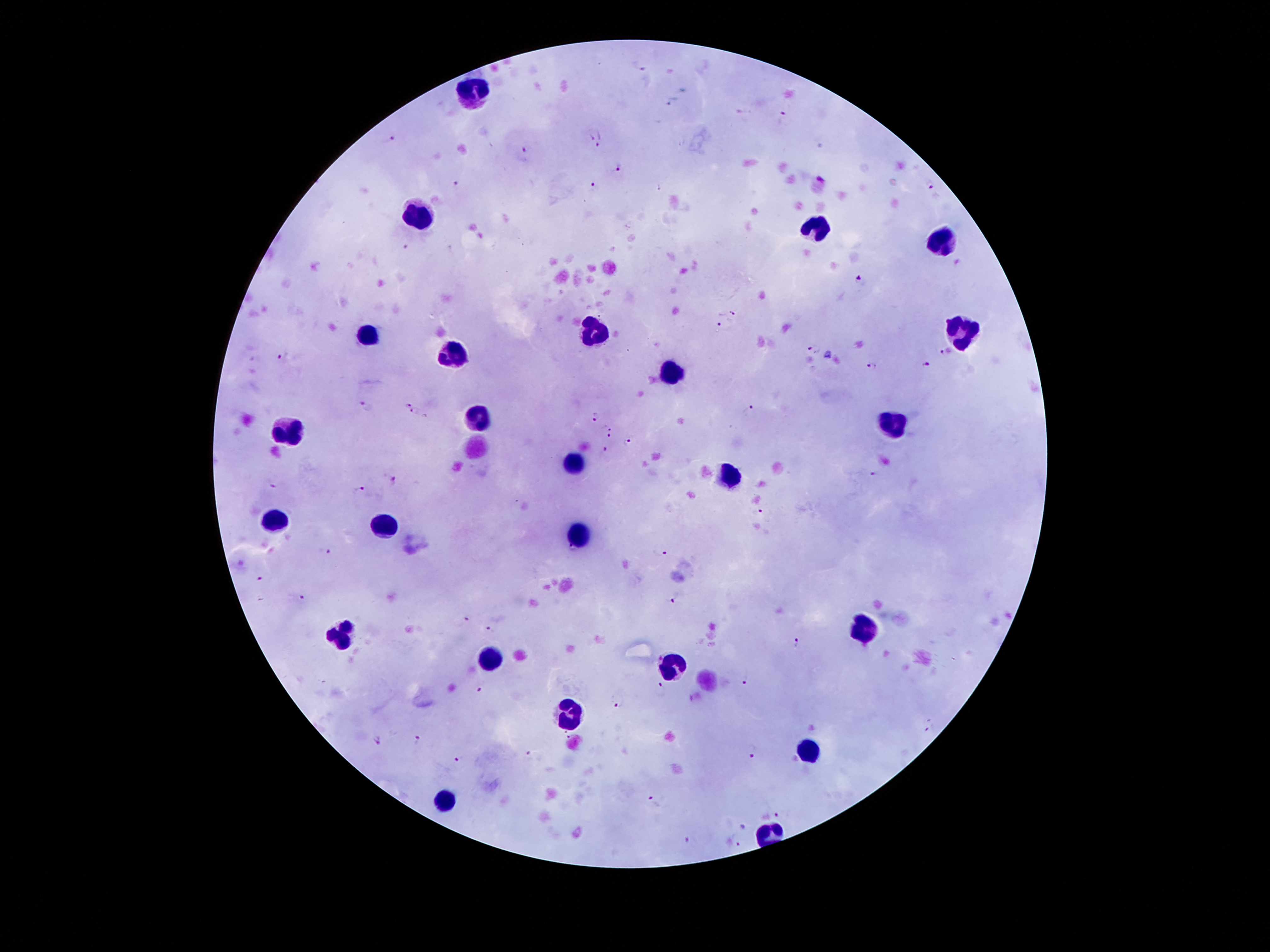 Approximate object centers, in pixels from the top-left corner. Malaria parasite locations: (x=640, y=66), (x=783, y=115), (x=389, y=139), (x=597, y=140), (x=524, y=154), (x=619, y=163), (x=457, y=185), (x=593, y=185), (x=931, y=188), (x=405, y=247), (x=862, y=278), (x=734, y=313), (x=721, y=326), (x=813, y=349), (x=946, y=352), (x=283, y=358), (x=871, y=366), (x=927, y=366), (x=364, y=406), (x=413, y=411), (x=752, y=411), (x=593, y=417), (x=610, y=425), (x=610, y=436), (x=629, y=441), (x=604, y=450), (x=872, y=473), (x=394, y=480), (x=271, y=484), (x=359, y=488), (x=759, y=509), (x=326, y=552), (x=660, y=552), (x=260, y=578), (x=301, y=598), (x=676, y=600), (x=465, y=618), (x=490, y=626), (x=797, y=644), (x=748, y=681), (x=660, y=686), (x=480, y=691), (x=616, y=702), (x=929, y=727), (x=417, y=740), (x=377, y=741), (x=529, y=754), (x=751, y=756), (x=459, y=761), (x=652, y=802), (x=778, y=813), (x=744, y=825), (x=691, y=840), (x=734, y=842). Leukocyte locations: (x=472, y=91), (x=418, y=219), (x=818, y=227), (x=938, y=243), (x=590, y=331), (x=958, y=332), (x=368, y=333), (x=454, y=355), (x=670, y=374), (x=478, y=421), (x=892, y=422), (x=288, y=435), (x=476, y=447), (x=574, y=463), (x=730, y=478), (x=278, y=519), (x=388, y=527), (x=582, y=534), (x=864, y=627), (x=340, y=635), (x=487, y=662), (x=671, y=666), (x=567, y=714), (x=808, y=751), (x=447, y=799). Patient malaria status: infected with Plasmodium falciparum. Smartphone photograph taken through the microscope eyepiece. Image is 1270×952 pixels. Thick blood smear. 100x magnification. Single field of view. Giemsa stain.